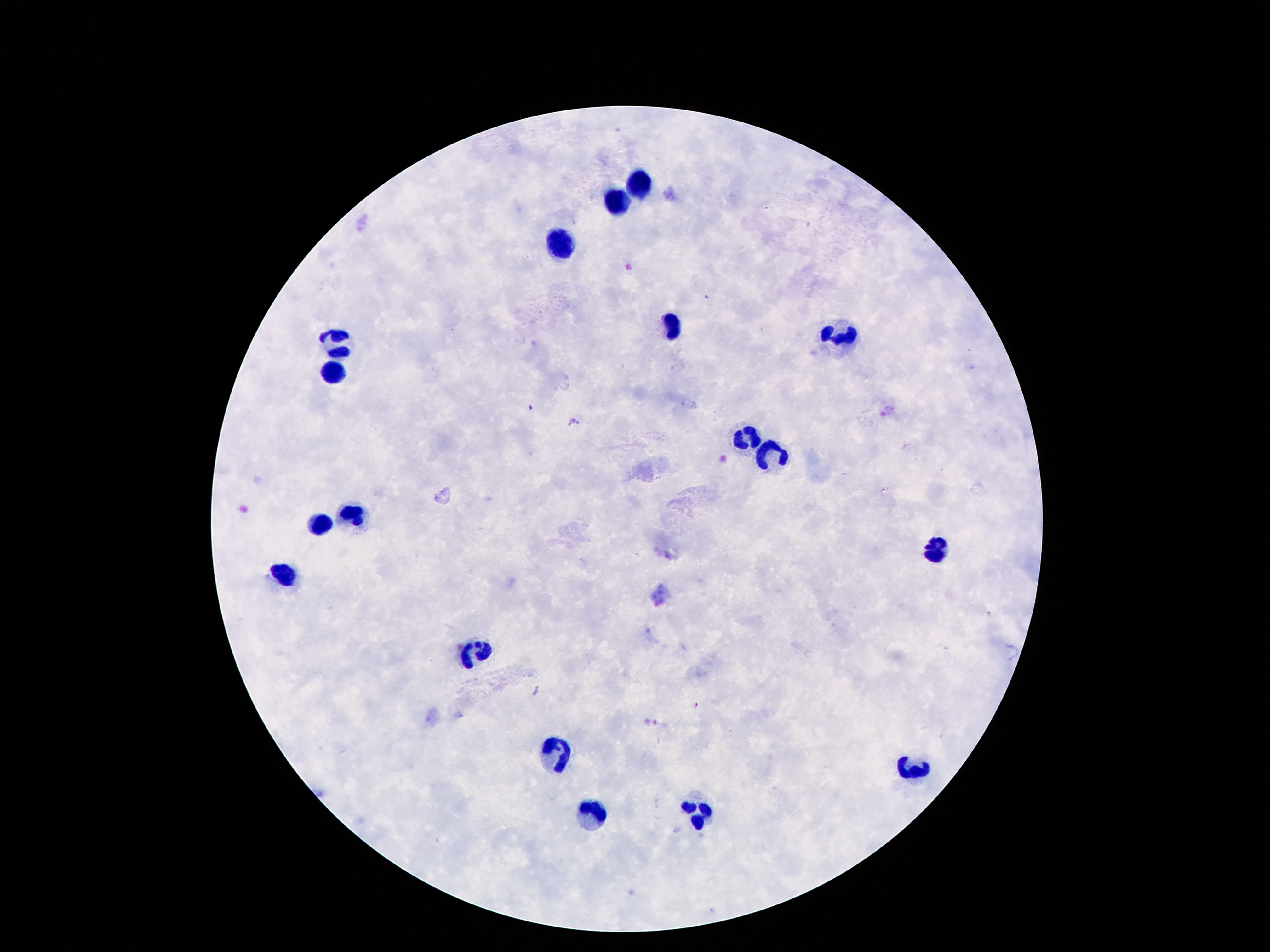

Approximate centers as (x, y) in pixels. Leukocyte locations: (641, 185), (618, 205), (561, 242), (672, 328), (336, 340), (844, 342), (336, 373), (753, 436), (770, 445), (354, 514), (321, 522), (934, 553), (283, 576), (481, 651), (553, 748), (917, 770), (590, 813), (700, 813). Image is 1270×952 pixels. Photographed through the microscope eyepiece with a smartphone camera. Giemsa stain. Thick peripheral-blood smear. 100x magnification. Patient malaria status: uninfected. One field from this slide.